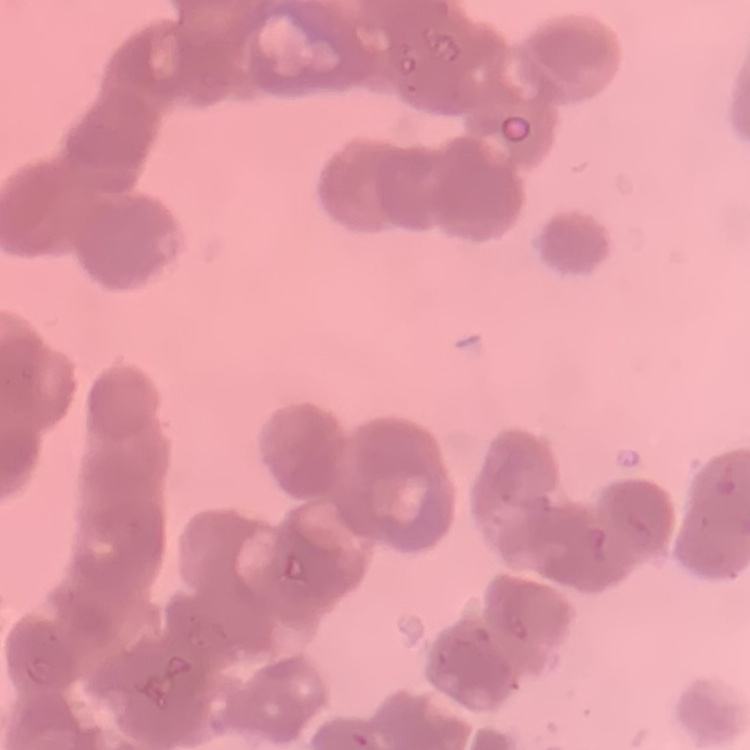

The erythrocytes show rouleaux formation. Thin blood film. One tile cut from a larger photomicrograph. Field's or Giemsa stain.